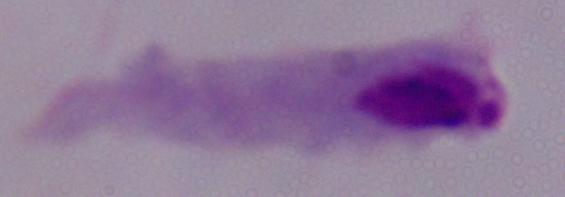

A trichomonad is shown. Photomicrograph. Captured at 1000x magnification.